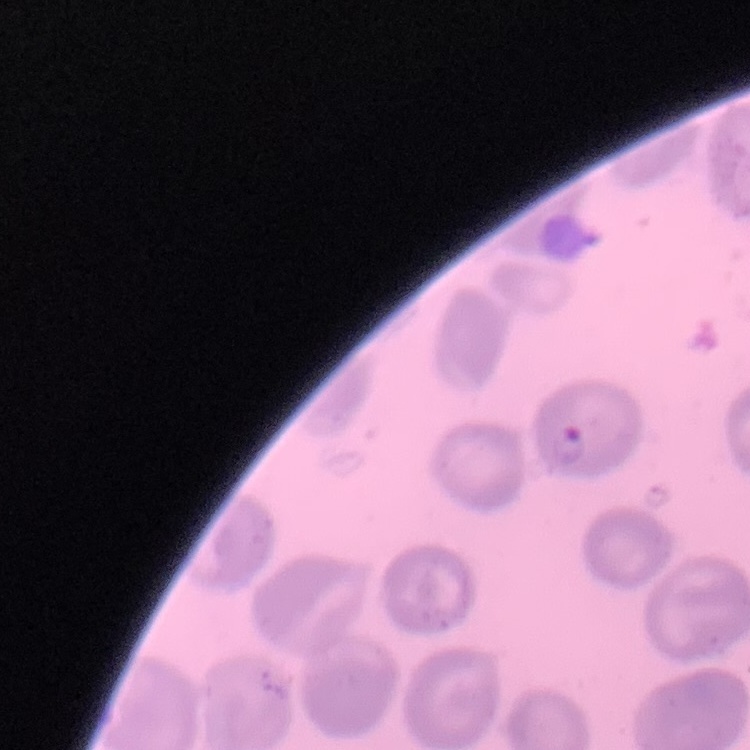

The red blood cells show no rouleaux formation. Thin blood film. Square crop of a larger photomicrograph. Stained with either Field's or Giemsa.